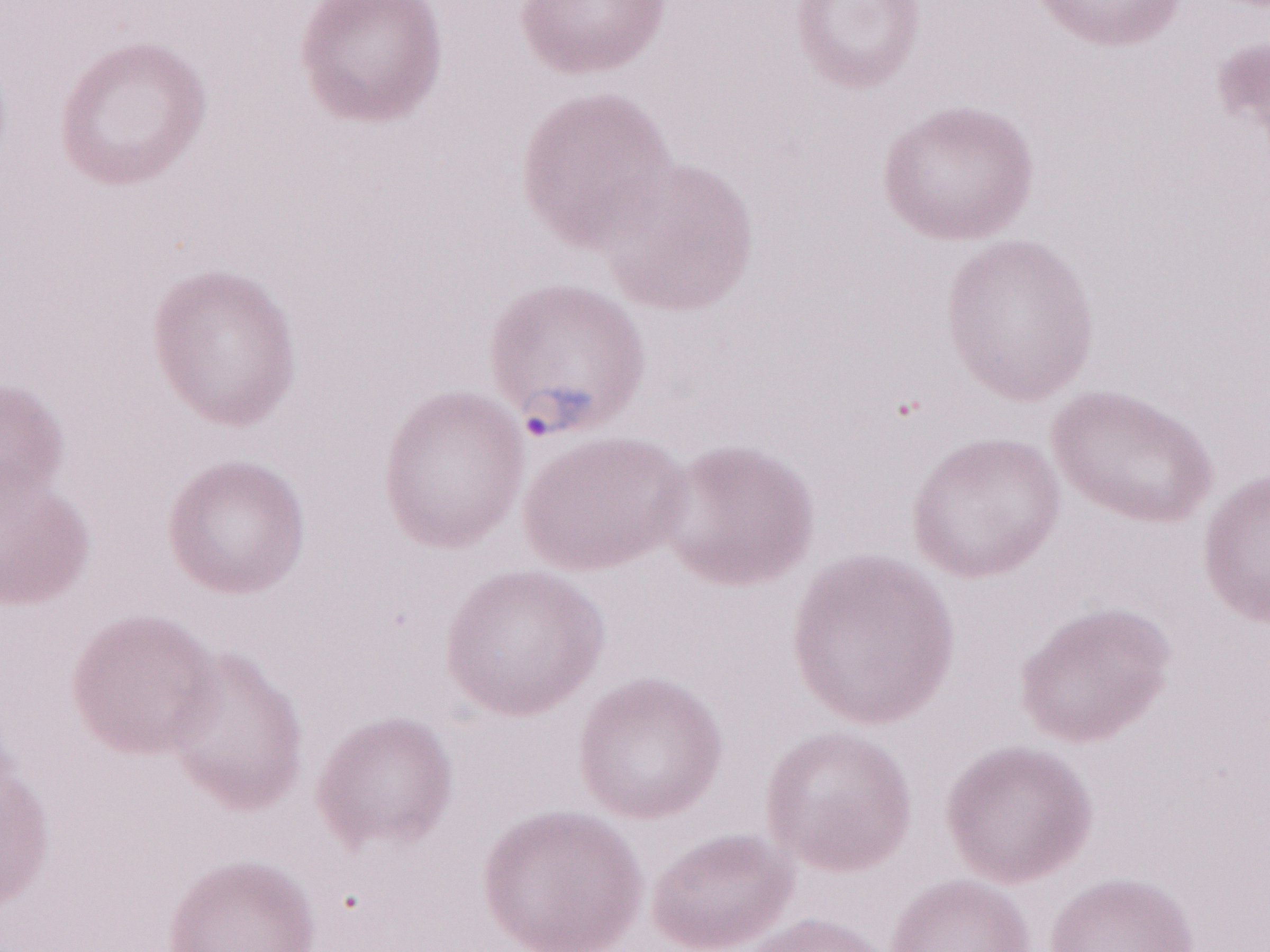

1,000x magnification. Single field of view. Image is 1270×952 pixels. Olympus BX43 microscope, Olympus DP73 camera. Thin blood smear. May-Grünwald-Giemsa-stained preparation. Patient diagnosis: malaria infection.